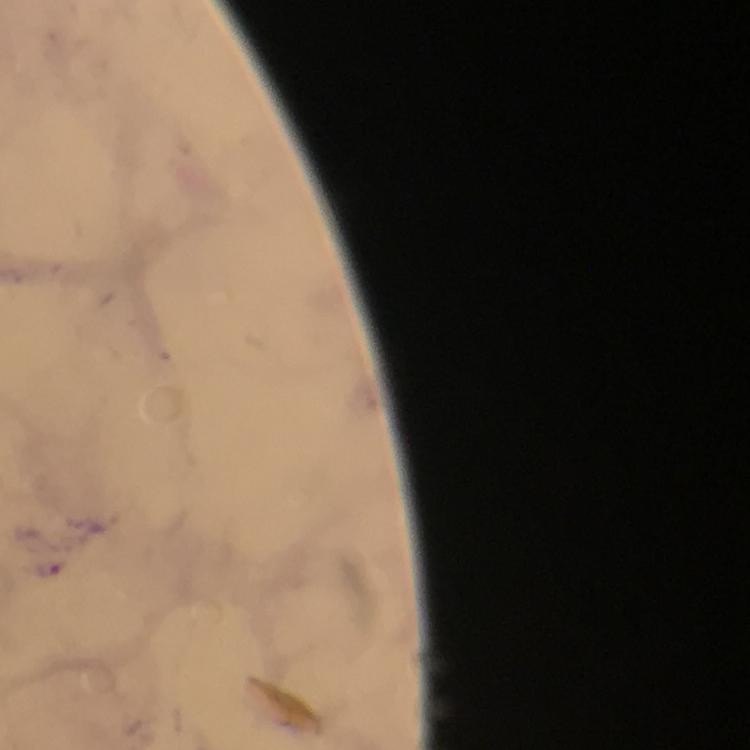

stain = Giemsa
image size = 750×750 pixels
capture = smartphone camera through the microscope
malaria parasite locations = approximate centers as [x, y] in pixels: [50, 564]
magnification = 100x
context = from a diagnostic examination for malaria
preparation = thick blood smear
cropped from = a single field of view
immersion oil = used